Locate every malaria parasite.
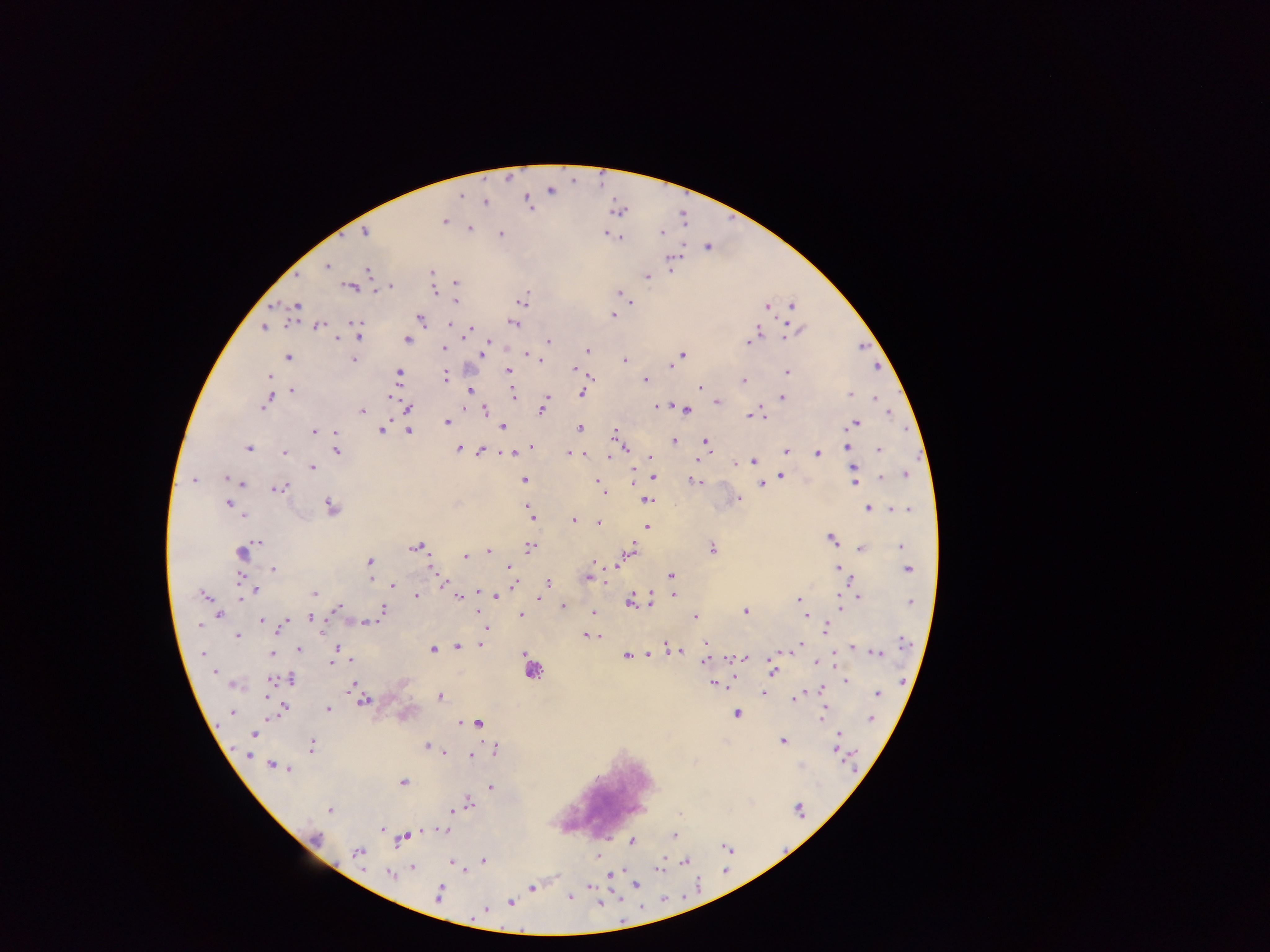
Approximate centers as [x, y] in pixels.
Malaria parasites: [551, 191], [462, 196], [486, 202], [528, 202], [444, 221], [470, 228], [365, 232], [660, 232], [606, 233], [500, 235], [620, 237], [707, 247], [675, 258], [327, 267], [671, 269], [369, 271], [431, 272], [297, 276], [647, 277], [455, 283], [349, 287], [392, 287], [434, 291], [621, 293], [522, 301], [456, 303], [632, 304], [297, 305], [791, 305], [766, 306], [614, 315], [420, 318], [356, 323], [450, 324], [514, 324], [318, 326], [264, 327], [471, 329], [757, 331], [799, 331], [469, 333], [786, 336], [360, 337], [338, 338], [407, 340], [488, 342], [549, 342], [748, 343], [444, 348], [587, 350], [482, 354], [528, 355], [682, 355], [287, 357], [353, 360], [625, 360], [672, 365], [574, 368], [507, 371], [787, 372], [399, 373], [269, 377], [591, 377], [446, 378], [645, 380], [743, 381], [700, 388], [292, 390], [470, 391], [581, 394], [850, 394], [391, 396], [513, 396], [547, 397], [782, 397], [877, 398], [718, 402], [266, 403], [545, 405], [657, 406], [408, 407], [484, 409], [542, 410], [685, 410], [362, 411], [751, 417], [763, 418], [447, 422], [855, 424], [503, 427], [580, 428], [313, 431], [382, 431], [409, 431], [615, 431], [336, 432], [674, 442], [705, 442], [531, 446], [847, 446], [249, 448], [458, 449], [481, 450], [879, 450], [336, 451], [284, 452], [786, 452], [509, 453], [569, 453], [584, 454], [817, 454], [608, 457], [651, 457], [697, 460], [753, 461], [736, 464], [312, 468], [854, 469], [633, 471], [906, 475], [781, 476], [227, 478], [654, 478], [882, 478], [524, 480], [194, 481], [597, 481], [694, 481], [855, 482], [242, 484], [762, 484], [600, 487], [279, 489], [604, 493], [739, 498], [647, 501], [228, 504], [331, 507], [529, 509], [868, 509], [902, 509], [244, 516], [532, 516], [574, 520], [598, 523], [647, 527], [831, 539], [259, 542], [900, 545], [415, 547], [531, 547], [712, 548], [861, 548], [631, 550], [488, 551], [242, 553], [466, 556], [594, 561], [369, 562], [614, 567], [509, 568], [838, 568], [274, 569], [433, 570], [908, 570], [671, 575], [588, 577], [239, 578], [371, 579], [548, 582], [442, 584], [393, 585], [513, 586], [256, 590], [314, 593], [479, 593], [203, 595], [416, 596], [496, 596], [673, 596], [242, 597], [459, 597], [858, 597], [539, 599], [798, 599], [910, 602], [630, 603], [839, 603], [650, 605], [563, 606], [339, 608], [383, 610], [746, 611], [478, 612], [593, 612], [220, 614], [521, 615], [806, 616], [311, 617], [695, 618], [261, 620], [366, 623], [285, 624], [199, 625], [826, 628], [487, 629], [587, 635], [237, 636], [903, 642], [705, 643], [480, 645], [799, 646], [457, 647], [336, 648], [668, 648], [852, 649], [299, 650], [432, 650], [791, 650], [676, 651], [877, 653], [202, 654], [273, 654], [648, 654], [626, 656], [743, 658], [706, 659], [350, 660], [817, 663], [331, 664], [773, 669], [215, 671], [533, 671], [290, 679], [271, 681], [846, 681], [713, 684], [352, 685], [820, 691], [764, 693], [877, 694], [440, 697], [795, 698], [364, 701], [283, 709], [328, 709], [232, 712], [736, 714], [822, 714], [872, 719], [477, 722], [461, 723], [253, 734], [839, 739], [782, 741], [312, 746], [427, 746], [837, 748], [495, 750], [444, 752], [470, 755], [249, 756], [272, 765], [280, 767], [800, 767], [287, 769], [403, 782], [491, 787], [468, 803], [798, 809], [330, 810], [451, 811], [679, 814], [382, 828], [444, 830], [675, 836], [405, 837], [317, 838], [632, 841], [727, 848], [358, 852], [483, 861], [685, 862], [451, 863], [412, 867], [660, 869], [390, 874], [611, 875], [636, 884], [591, 886], [532, 888], [439, 893], [569, 896], [511, 902], [599, 903], [486, 909].

{
  "leukocyte_locations": "approximate centers as [x, y] in pixels: [606, 792]",
  "preparation": "thick blood film",
  "image_size": "1270×952 pixels",
  "field_of_view": "single",
  "country": "Ghana",
  "capture": "mobile-phone photograph through a microscope"
}